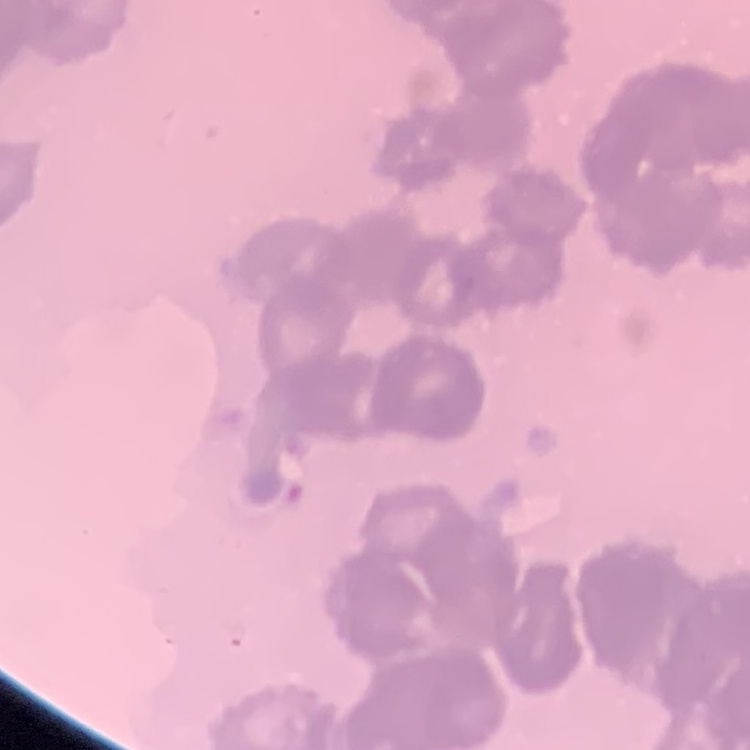

erythrocyte morphology = rouleaux formation
stain = Field's or Giemsa
preparation = thin blood film
image type = square crop of a larger photomicrograph